Assess this cell for malaria.
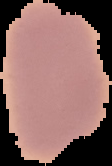

It is uninfected.

image_size: 112×166 pixels
image_type: segmented cell region with the area outside set to black
preparation: thin blood smear